State the blood parasite species.
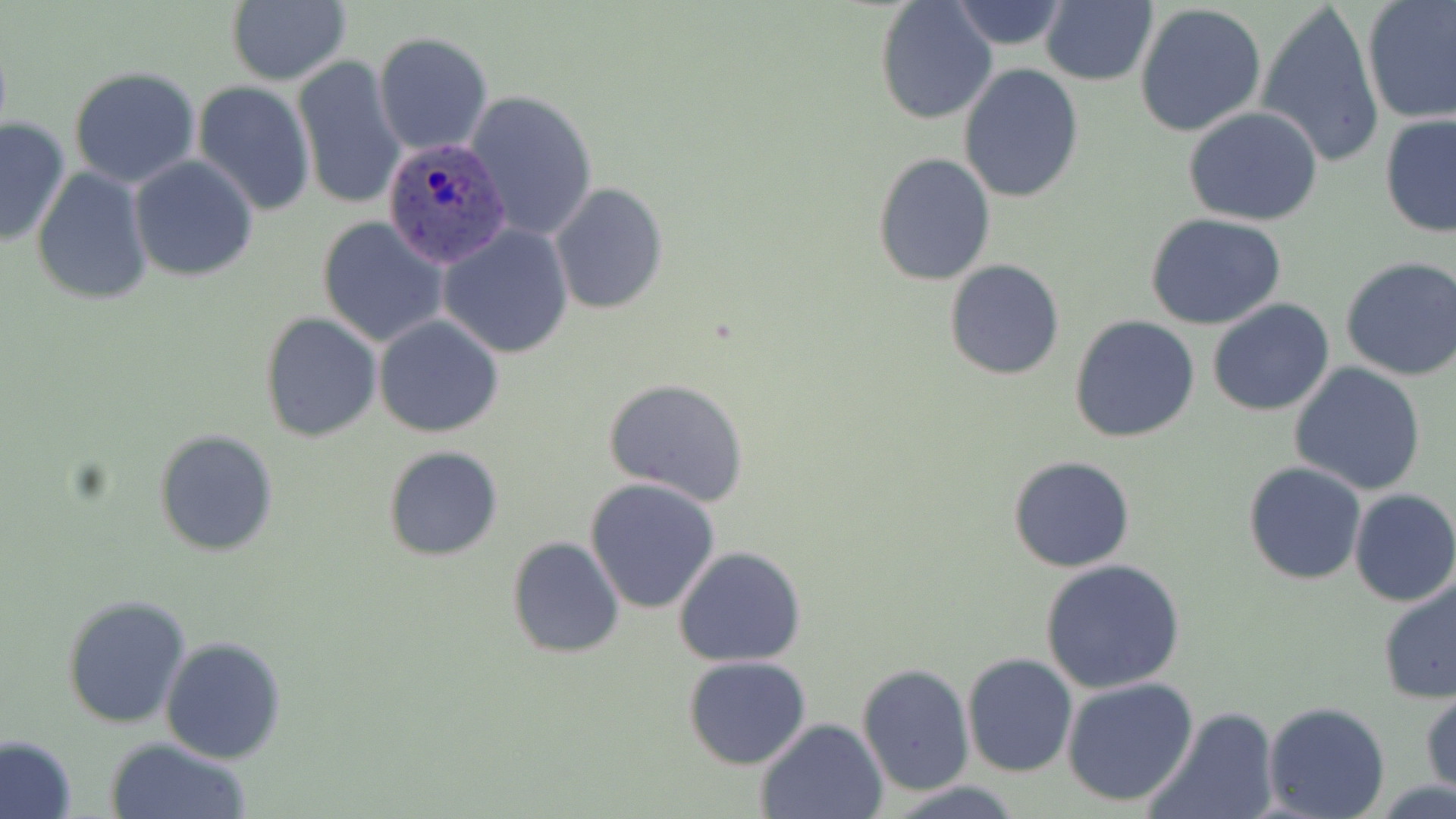

Plasmodium ovale.

Summary:
  - Coordinate format: approximate bounding boxes as (x1,y1)-(x2,y2) corner pairs in pixels
  - Uninfected red blood cell locations: (224,0)-(350,87), (875,1)-(999,123), (946,1)-(1073,52), (1256,1)-(1387,169), (1040,2)-(1157,86), (1360,2)-(1456,125), (1134,3)-(1267,140), (372,32)-(492,156), (292,55)-(405,210), (958,64)-(1085,203), (68,68)-(201,188), (192,80)-(315,217), (465,89)-(599,244), (1184,108)-(1323,226), (1378,114)-(1456,237), (0,116)-(74,249), (872,152)-(997,286), (128,156)-(259,281), (31,167)-(154,305), (550,183)-(668,316), (1147,214)-(1287,330), (317,216)-(451,349), (438,224)-(574,359), (1340,256)-(1456,382), (944,259)-(1064,380), (1206,299)-(1336,417), (260,312)-(382,443), (374,314)-(506,438), (1069,316)-(1201,443), (1288,364)-(1427,497), (603,378)-(750,506), (154,429)-(277,557), (384,446)-(503,561), (1007,455)-(1136,573), (1243,462)-(1366,586), (585,478)-(723,615), (1348,489)-(1456,607), (506,535)-(627,659), (673,546)-(806,665), (1039,558)-(1186,693), (1377,574)-(1456,704), (61,595)-(191,730), (160,635)-(287,764), (961,652)-(1077,776), (684,656)-(813,770), (856,664)-(975,794), (1061,676)-(1202,808), (1421,688)-(1455,795), (1263,702)-(1391,819), (1145,707)-(1280,819), (756,717)-(887,819), (0,734)-(77,819), (104,737)-(253,819), (885,781)-(1027,818)
  - Plasmodium ovale-infected red blood cell locations: (379,136)-(503,265)
  - Image size: 1456×819 pixels
  - Modality: optical microscopy
  - Field of view: single
  - Stain: May-Grünwald-Giemsa
  - Magnification: 1000x
  - Preparation: thin blood film